Assess the morphology of the erythrocytes.
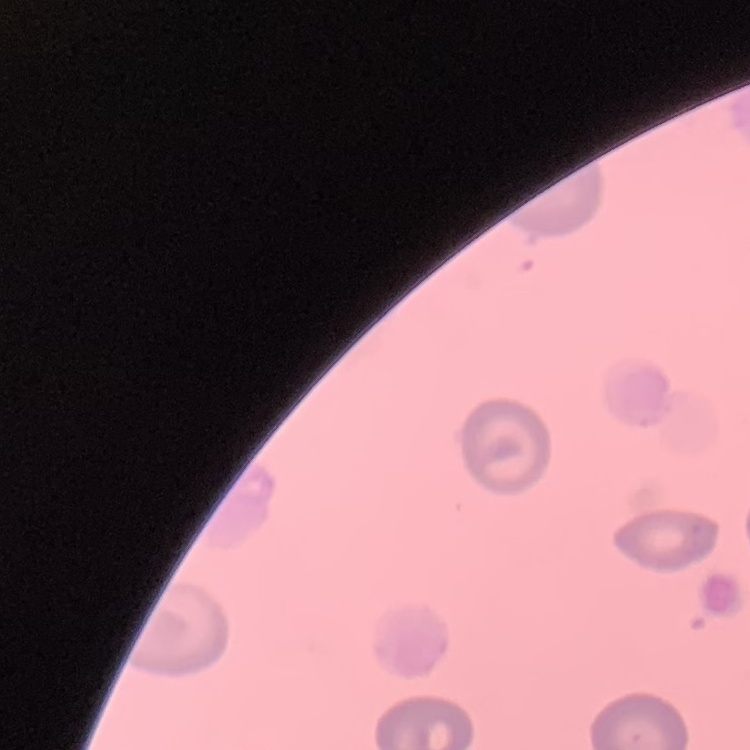
They show no rouleaux formation.

stain = Field's or Giemsa
image type = square crop of a larger photomicrograph
preparation = thin peripheral smear